Find the red blood cells that are infected with Plasmodium falciparum, and any of indeterminate infection status.
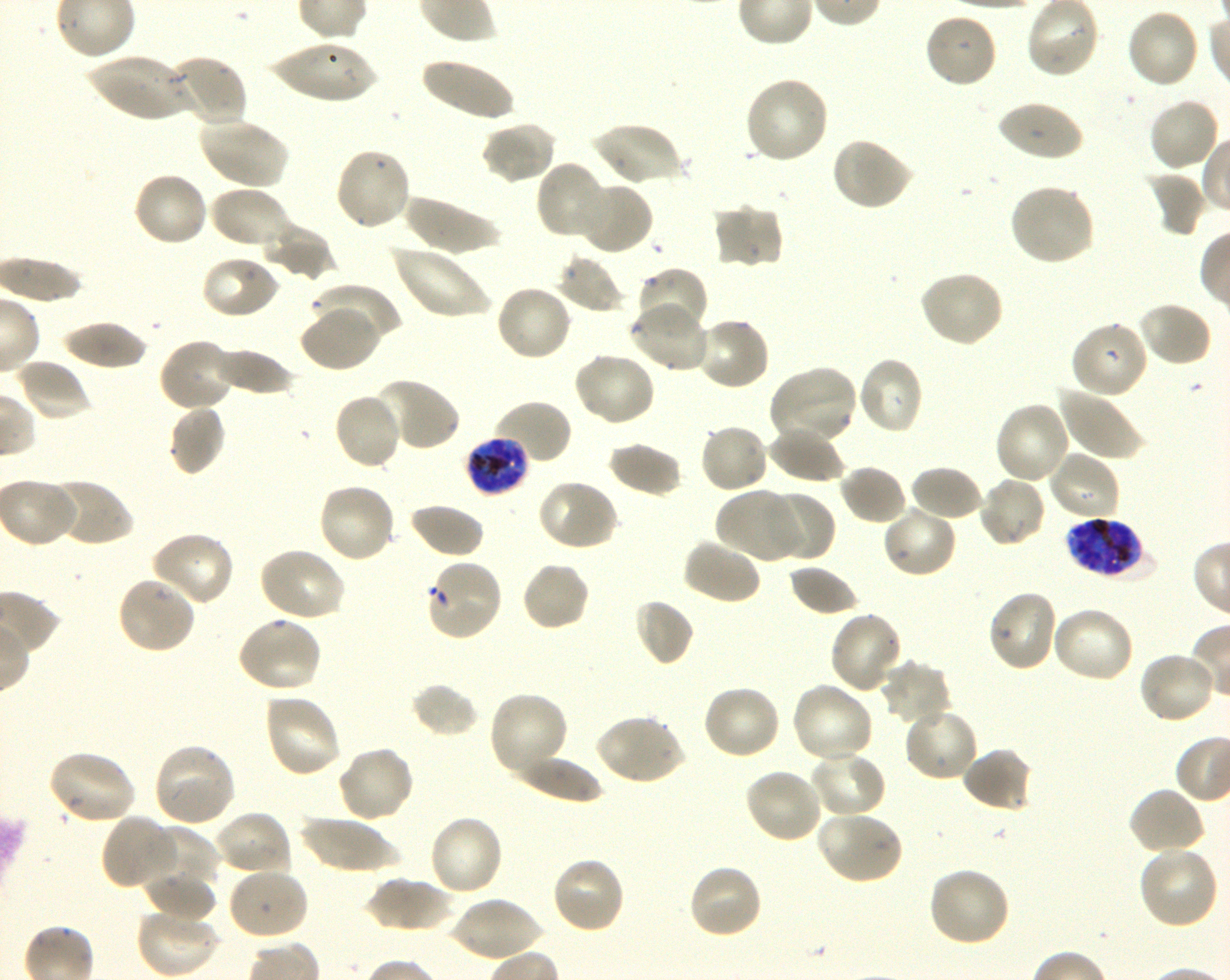

Approximate bounding boxes as [x1, y1, x2, y2] in pixels. Not every red blood cell is marked. A life-cycle stage — or a range of stages, where the recorded stages span more than one — follows each staged infected red blood cell.
Infected red blood cells: [465, 436, 529, 494] late trophozoite to late schizont; [1066, 515, 1149, 579] schizont.
Red blood cells of indeterminate infection status: [425, 559, 504, 640].

Locations of uninfected red blood cells: [1125, 8, 1200, 89], [923, 12, 999, 89], [268, 42, 381, 104], [83, 54, 193, 122], [163, 54, 249, 125], [419, 55, 515, 123], [743, 76, 830, 165], [1147, 97, 1221, 173], [996, 99, 1083, 163], [198, 118, 289, 190], [480, 120, 558, 186], [589, 121, 683, 188], [830, 136, 915, 212], [333, 147, 413, 232], [536, 160, 612, 241], [1144, 170, 1207, 237], [132, 171, 209, 248], [573, 180, 653, 256], [1009, 182, 1095, 267], [208, 186, 294, 251], [401, 193, 502, 254], [711, 204, 784, 270], [260, 221, 334, 280], [391, 244, 491, 320], [557, 253, 624, 313], [200, 254, 280, 321], [633, 265, 708, 337], [918, 269, 1005, 348], [309, 282, 402, 348], [494, 283, 573, 362], [628, 301, 709, 372], [1137, 301, 1213, 368], [300, 304, 383, 372], [694, 316, 771, 392], [59, 319, 149, 370], [1070, 320, 1149, 399], [158, 338, 239, 413], [211, 347, 298, 397], [572, 351, 657, 427], [856, 356, 924, 435], [15, 358, 92, 422], [767, 366, 859, 445], [371, 377, 460, 452], [1057, 385, 1146, 462], [333, 392, 404, 472], [489, 399, 573, 467], [994, 401, 1071, 486], [168, 404, 227, 476], [699, 421, 770, 494], [766, 426, 846, 483], [606, 441, 683, 498], [1047, 449, 1122, 522], [838, 464, 908, 526], [909, 464, 985, 523], [977, 476, 1047, 549], [537, 477, 619, 551], [46, 478, 134, 548], [316, 482, 397, 564], [715, 486, 803, 563], [765, 489, 834, 561], [408, 502, 485, 559], [881, 503, 958, 579], [148, 531, 235, 608], [681, 538, 762, 606], [257, 545, 345, 623], [521, 560, 591, 632], [788, 563, 861, 617], [116, 575, 198, 655], [987, 589, 1060, 672], [633, 598, 694, 667], [1051, 605, 1136, 684], [828, 610, 905, 695], [235, 617, 322, 695], [1137, 651, 1218, 726], [880, 658, 954, 727], [790, 681, 876, 765], [410, 682, 479, 737], [700, 683, 781, 761], [488, 690, 569, 780], [263, 692, 342, 779], [902, 705, 979, 783], [595, 713, 686, 786], [152, 742, 237, 828], [336, 746, 415, 824], [960, 747, 1034, 813], [46, 749, 135, 825], [809, 750, 886, 820], [512, 753, 607, 804], [743, 768, 824, 845], [1127, 786, 1206, 857], [213, 810, 292, 878], [813, 810, 904, 885], [100, 814, 178, 891], [427, 814, 504, 898], [298, 815, 399, 873], [144, 826, 219, 890], [1137, 844, 1220, 929], [550, 856, 626, 935], [686, 863, 764, 941], [927, 865, 1011, 947], [226, 866, 310, 941], [144, 870, 218, 924], [363, 876, 459, 932], [451, 895, 543, 962], [135, 908, 219, 977]. Image is 1230×980 pixels. Thin blood smear. One field from this slide. Donor blood group O+. Oil immersion, 100x objective (numerical aperture 1.30). Giemsa stain. Shaking in-vitro culture of Plasmodium falciparum strain 3D7.